Locate every blood parasite and identify its species.
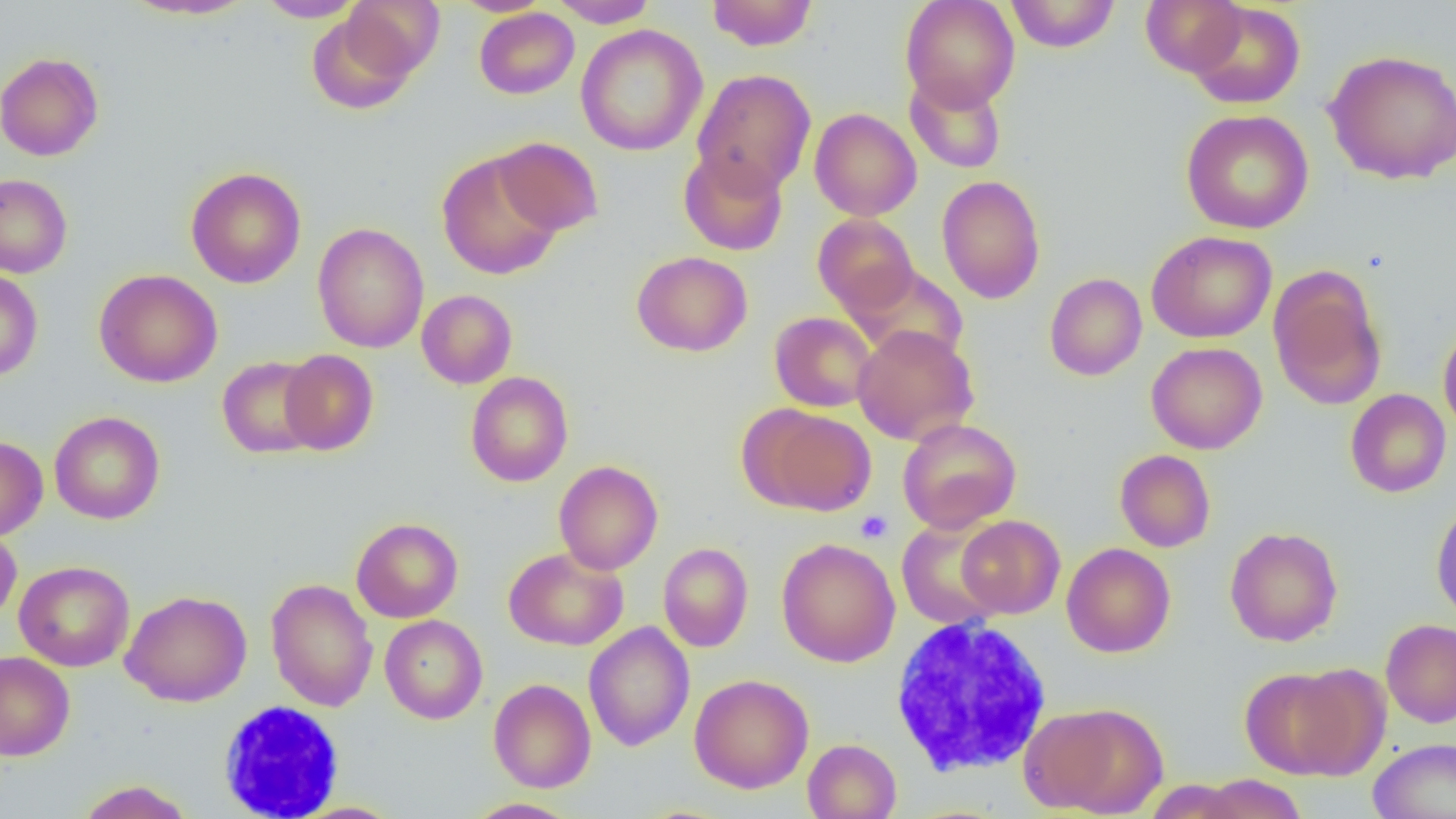

No blood parasites seen.

{
  "slide_level_diagnosis": "negative for blood parasites",
  "magnification": "1000x",
  "field_of_view": "one of a larger specimen",
  "preparation": "thin blood smear",
  "platelet_locations": "approximate bounding boxes as (x1, y1, x2, y2) in pixels: (855, 510, 893, 543)",
  "modality": "optical microscopy",
  "uninfected_red_blood_cell_locations": "approximate bounding boxes as (x1, y1, x2, y2) in pixels: (120, 0, 257, 21), (254, 0, 365, 22), (451, 0, 553, 16), (548, 0, 659, 27), (706, 0, 818, 51), (900, 0, 1020, 112), (1004, 0, 1121, 52), (1140, 0, 1246, 76), (341, 1, 444, 82), (1187, 3, 1306, 109), (474, 8, 579, 99), (306, 12, 419, 115), (575, 24, 708, 157), (1323, 49, 1456, 185), (0, 52, 104, 161), (692, 68, 816, 195), (904, 73, 1007, 174), (809, 108, 922, 221), (1180, 109, 1314, 234), (494, 137, 604, 236), (678, 150, 788, 255), (437, 151, 564, 280), (186, 167, 306, 288), (0, 173, 72, 278), (936, 175, 1046, 304), (812, 213, 919, 316), (313, 223, 429, 353), (1146, 230, 1277, 344), (631, 251, 752, 357), (845, 264, 969, 365), (1269, 267, 1386, 411), (0, 268, 43, 381), (94, 268, 223, 388), (1044, 272, 1147, 381), (417, 289, 517, 389), (769, 312, 877, 412), (1438, 322, 1456, 438), (852, 325, 979, 446), (1145, 342, 1267, 454), (279, 349, 379, 455), (217, 356, 322, 459), (465, 371, 574, 487), (1345, 389, 1451, 498), (747, 405, 876, 516), (49, 411, 165, 524), (897, 418, 1021, 533), (0, 436, 48, 540), (1114, 449, 1216, 552), (553, 460, 663, 574), (1431, 498, 1456, 623), (956, 515, 1065, 618), (351, 517, 463, 623), (896, 518, 1006, 630), (0, 526, 21, 624), (1224, 526, 1343, 647), (776, 538, 901, 667), (658, 542, 753, 652), (1061, 542, 1175, 658), (504, 547, 629, 651), (14, 560, 135, 671), (265, 578, 378, 712), (120, 589, 252, 707), (380, 614, 487, 724), (1380, 619, 1456, 728), (583, 621, 695, 752), (0, 651, 75, 761), (1240, 666, 1363, 780), (689, 674, 814, 794), (488, 678, 596, 793), (1021, 701, 1169, 817), (1368, 737, 1456, 819), (802, 738, 901, 819), (1197, 774, 1308, 819), (1142, 779, 1249, 818), (75, 780, 195, 819), (465, 798, 580, 819), (288, 802, 405, 818)",
  "white_blood_cell_locations": "approximate bounding boxes as (x1, y1, x2, y2) in pixels: (889, 615, 1053, 777), (218, 700, 346, 819)",
  "image_size": "1456×819 pixels"
}